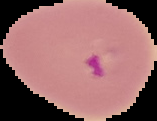 Result: malaria parasites detected. Image is 157×121 pixels. The area outside the segmented cell region is set to black. From a thin blood smear.